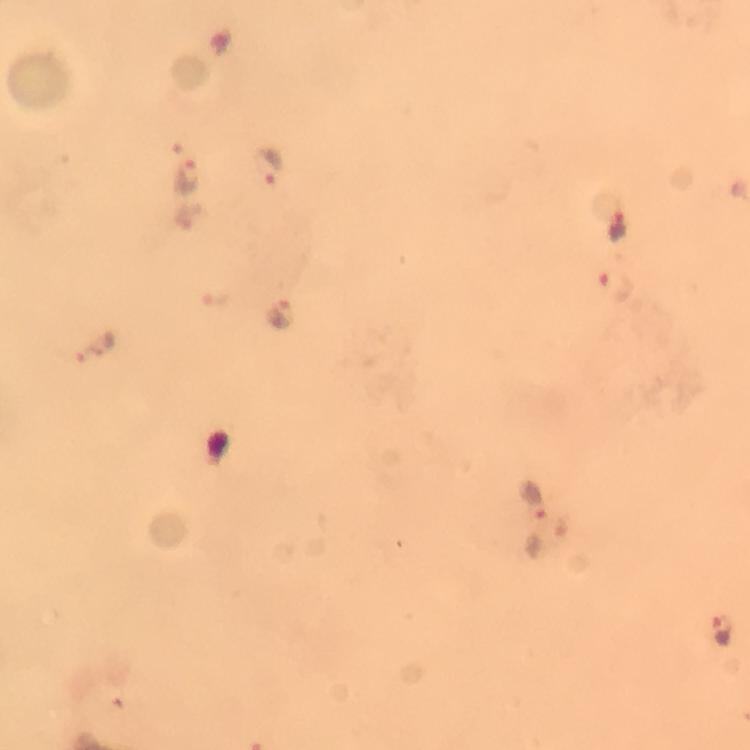

stain = Giemsa
immersion oil = used
cropped from = one field of view
malaria parasite locations = approximate centers as (x, y) in pixels: (271, 163), (187, 176), (617, 222), (616, 286), (220, 300), (282, 313), (536, 500), (721, 632)
capture = smartphone photograph through a microscope
preparation = thick blood film
context = from a malaria diagnostic workup
image size = 750×750 pixels
magnification = 100x